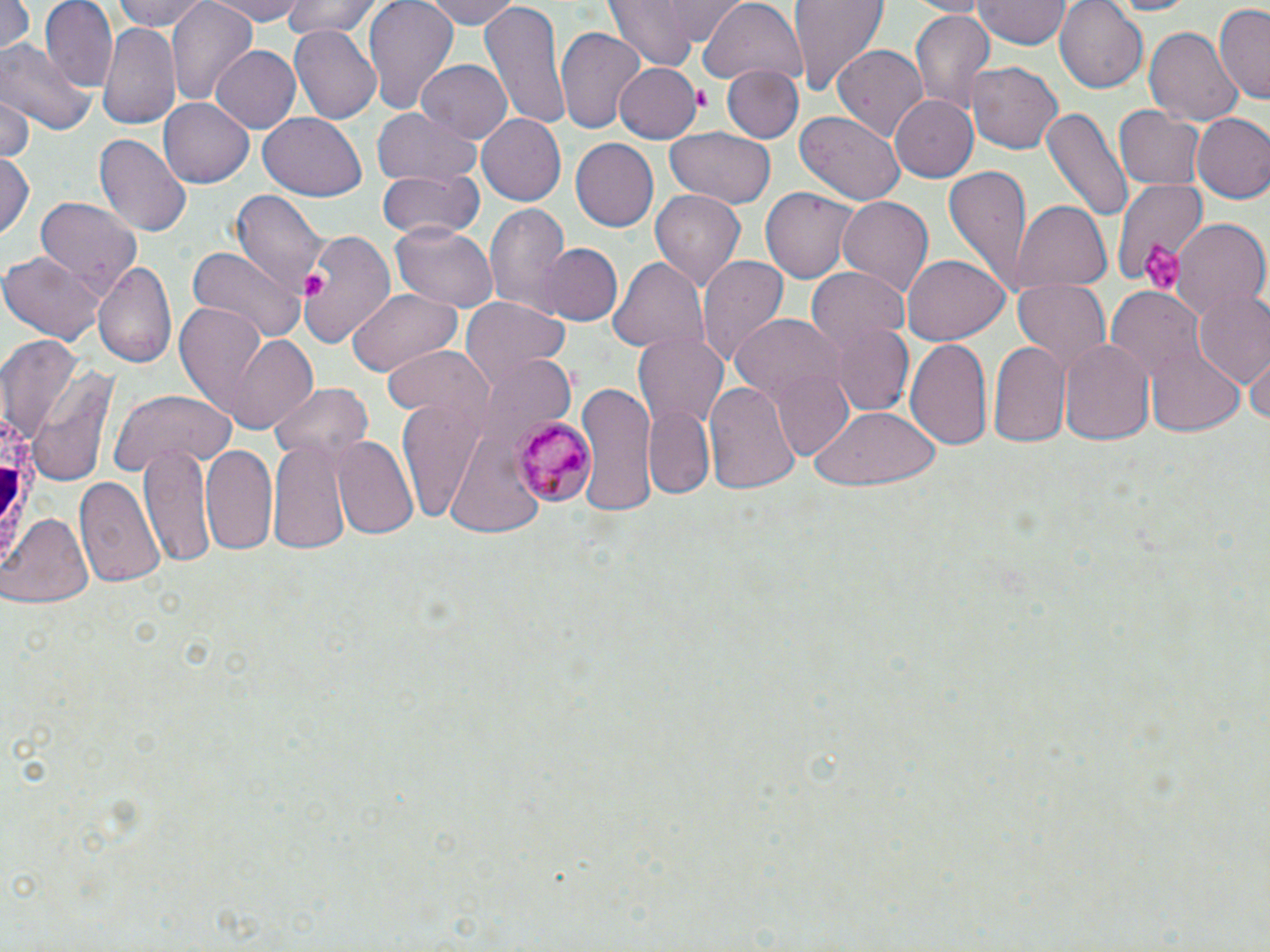

slide-level diagnosis = Plasmodium malariae
white blood cell locations = approximate bounding boxes as [x1, y1, x2, y2] in pixels: [0, 407, 46, 585]
image size = 1270×952 pixels
Plasmodium malariae-infected red blood cell locations = approximate bounding boxes as [x1, y1, x2, y2] in pixels: [512, 416, 590, 505]
magnification = 1000x
preparation = thin blood smear
modality = light microscopy
platelet locations = approximate bounding boxes as [x1, y1, x2, y2] in pixels: [692, 87, 709, 109], [1138, 238, 1184, 295], [303, 273, 325, 298]
field of view = one of a larger specimen
stain = May-Grünwald-Giemsa
uninfected red blood cell locations = approximate bounding boxes as [x1, y1, x2, y2] in pixels: [40, 0, 117, 88], [109, 0, 214, 34], [169, 0, 255, 104], [202, 0, 308, 24], [281, 0, 384, 41], [360, 0, 460, 116], [419, 0, 523, 28], [479, 0, 568, 130], [603, 0, 732, 67], [790, 0, 889, 92], [972, 0, 1069, 50], [1056, 0, 1149, 92], [1103, 0, 1199, 16], [0, 1, 31, 55], [700, 2, 807, 87], [1214, 4, 1270, 104], [909, 10, 995, 113], [99, 19, 182, 131], [1144, 24, 1244, 127], [288, 28, 381, 123], [556, 28, 646, 135], [0, 37, 96, 134], [834, 44, 927, 142], [210, 45, 301, 134], [417, 60, 512, 144], [964, 61, 1065, 154], [613, 62, 702, 142], [722, 67, 802, 142], [0, 95, 34, 161], [890, 95, 977, 182], [160, 100, 253, 187], [1116, 104, 1203, 190], [1042, 106, 1132, 224], [373, 109, 484, 185], [793, 110, 906, 205], [1192, 112, 1270, 203], [257, 114, 367, 201], [477, 114, 565, 205], [665, 130, 775, 209], [94, 133, 191, 237], [569, 139, 657, 232], [0, 155, 36, 242], [943, 165, 1033, 290], [377, 170, 484, 238], [1114, 178, 1211, 286], [760, 188, 861, 281], [649, 189, 747, 294], [231, 190, 330, 294], [35, 196, 141, 295], [835, 196, 933, 297], [484, 202, 570, 314], [1011, 202, 1113, 293], [1168, 218, 1267, 321], [390, 221, 501, 312], [295, 229, 396, 346], [538, 242, 623, 327], [188, 246, 304, 342], [1, 251, 106, 345], [608, 256, 709, 355], [698, 256, 788, 371], [901, 256, 1010, 346], [93, 260, 177, 370], [805, 268, 911, 352], [1011, 278, 1109, 375], [347, 288, 462, 377], [1107, 288, 1200, 381], [1192, 289, 1270, 389], [461, 299, 569, 393], [173, 304, 270, 415], [730, 315, 844, 410], [821, 319, 913, 415], [216, 330, 320, 430], [634, 333, 725, 429], [1, 337, 83, 440], [905, 337, 994, 455], [988, 339, 1071, 449], [1059, 339, 1154, 447], [1146, 344, 1245, 435], [385, 345, 491, 428], [1244, 350, 1269, 432], [485, 354, 574, 435], [25, 368, 118, 488], [770, 370, 858, 460], [705, 379, 800, 496], [272, 382, 372, 464], [577, 385, 654, 518], [109, 388, 236, 474], [395, 396, 488, 521], [810, 405, 942, 491], [643, 407, 715, 498], [332, 437, 419, 541], [268, 438, 353, 558], [200, 441, 278, 554], [139, 442, 216, 567], [76, 475, 164, 586], [3, 512, 93, 610]